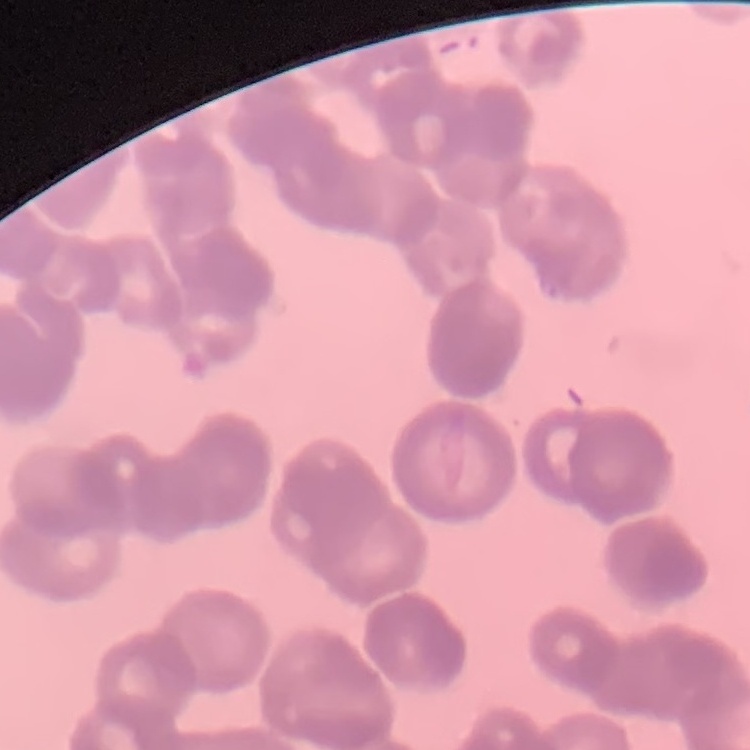

red_blood_cell_morphology: rouleaux formation
stain: Field's or Giemsa
preparation: thin blood smear
image_type: square crop of a larger photomicrograph